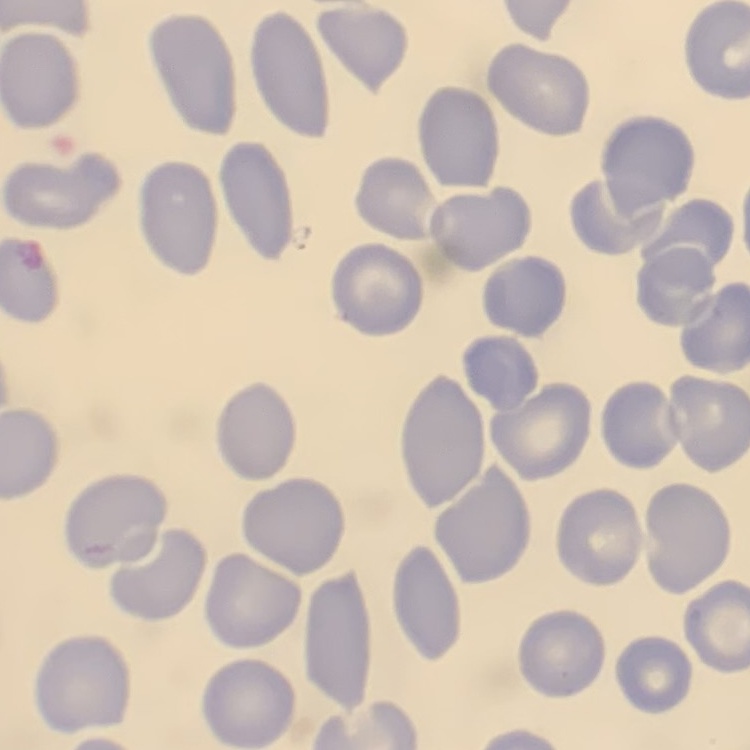

{
  "red_blood_cell_morphology": "no rouleaux formation",
  "stain": "Field's or Giemsa",
  "image_type": "square crop of a larger photomicrograph",
  "preparation": "thin blood smear"
}